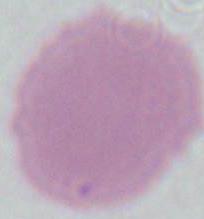
identification = erythrocyte
magnification = 1000x
modality = micrograph